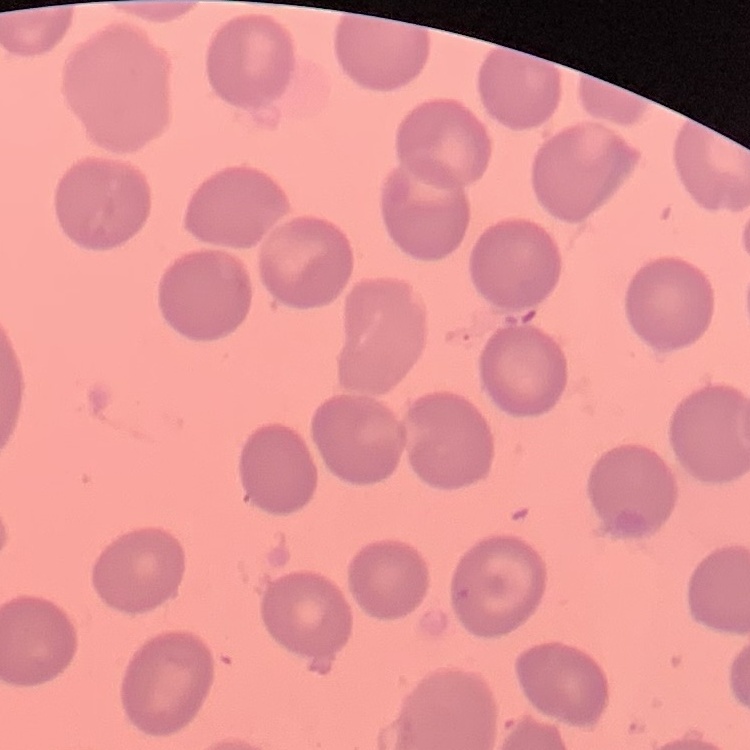

red_blood_cell_morphology: no rouleaux formation
image_type: one tile cut from a larger photomicrograph
preparation: thin blood film
stain: Field's or Giemsa